Comment on the morphology of the red blood cells.
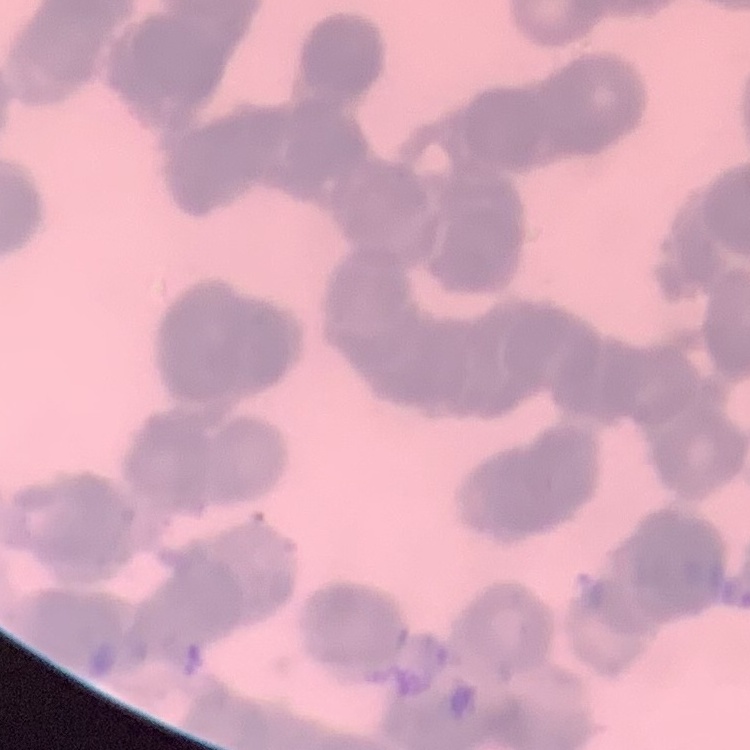
They show rouleaux formation.

Field's or Giemsa stain. One tile cut from a larger photomicrograph. Thin blood smear.